Assess the morphology of the red blood cells.
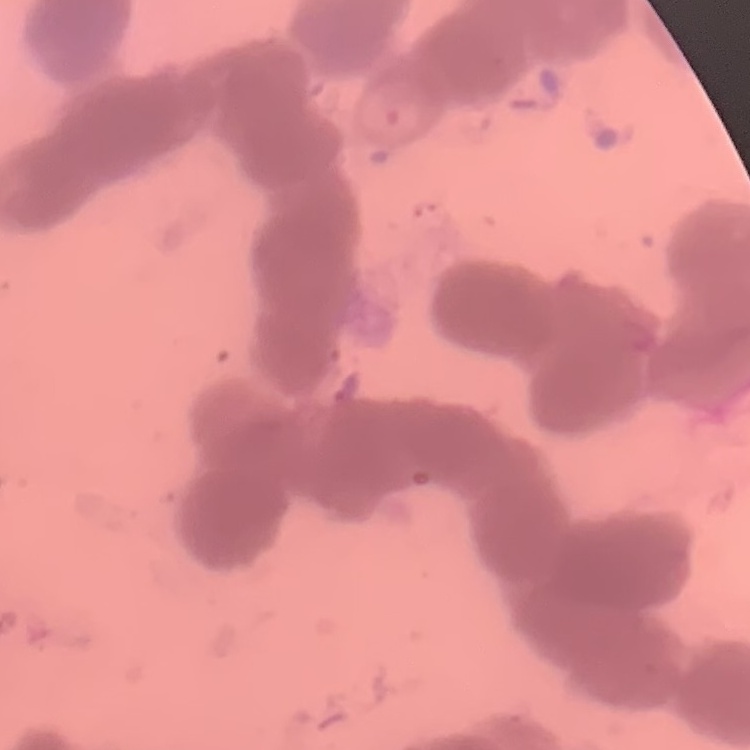

Rouleaux formation.

stain: Field's or Giemsa
image_type: square crop of a larger photomicrograph
preparation: thin blood smear